Name the blood parasite species.
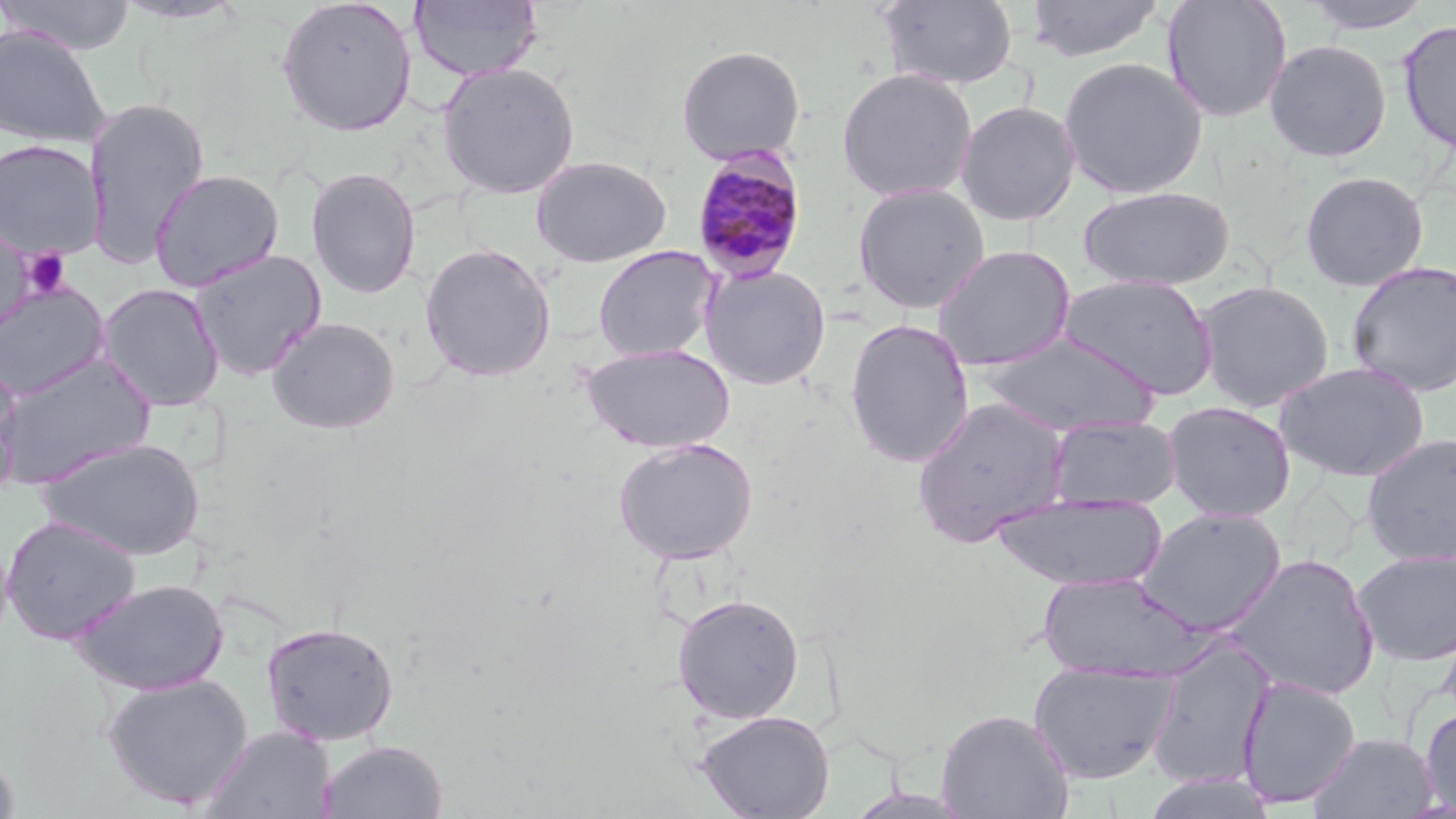
Plasmodium malariae.

field of view = one of a larger specimen
platelet locations = approximate bounding boxes as named x1/y1/x2/y2 corners in pixels: (x1=20, y1=248, x2=72, y2=299)
Plasmodium malariae-infected red blood cell locations = approximate bounding boxes as named x1/y1/x2/y2 corners in pixels: (x1=690, y1=147, x2=809, y2=284)
magnification = 1000x
stain = May-Grünwald-Giemsa
image size = 1456×819 pixels
modality = optical microscopy
preparation = thin blood smear
uninfected red blood cell locations = approximate bounding boxes as named x1/y1/x2/y2 corners in pixels: (x1=0, y1=0, x2=137, y2=55), (x1=112, y1=0, x2=248, y2=25), (x1=275, y1=0, x2=418, y2=138), (x1=408, y1=0, x2=544, y2=83), (x1=878, y1=0, x2=1019, y2=90), (x1=1025, y1=0, x2=1165, y2=63), (x1=1161, y1=0, x2=1293, y2=124), (x1=1298, y1=0, x2=1435, y2=34), (x1=1397, y1=19, x2=1456, y2=156), (x1=0, y1=24, x2=111, y2=148), (x1=1264, y1=39, x2=1392, y2=163), (x1=675, y1=44, x2=806, y2=166), (x1=1058, y1=56, x2=1209, y2=200), (x1=437, y1=61, x2=581, y2=200), (x1=836, y1=67, x2=978, y2=203), (x1=83, y1=97, x2=211, y2=269), (x1=955, y1=100, x2=1081, y2=226), (x1=0, y1=139, x2=106, y2=260), (x1=530, y1=155, x2=671, y2=268), (x1=305, y1=167, x2=421, y2=299), (x1=149, y1=169, x2=285, y2=292), (x1=1298, y1=170, x2=1430, y2=291), (x1=852, y1=182, x2=990, y2=313), (x1=1077, y1=186, x2=1237, y2=291), (x1=0, y1=219, x2=33, y2=342), (x1=419, y1=243, x2=556, y2=382), (x1=933, y1=244, x2=1076, y2=372), (x1=592, y1=245, x2=719, y2=362), (x1=189, y1=249, x2=327, y2=380), (x1=1345, y1=260, x2=1456, y2=397), (x1=700, y1=264, x2=832, y2=390), (x1=1057, y1=274, x2=1220, y2=401), (x1=1193, y1=279, x2=1335, y2=412), (x1=0, y1=281, x2=110, y2=400), (x1=96, y1=283, x2=226, y2=411), (x1=267, y1=316, x2=401, y2=434), (x1=844, y1=319, x2=975, y2=469), (x1=976, y1=333, x2=1161, y2=436), (x1=580, y1=343, x2=736, y2=453), (x1=0, y1=353, x2=156, y2=488), (x1=0, y1=360, x2=23, y2=496), (x1=1274, y1=361, x2=1431, y2=481), (x1=911, y1=396, x2=1071, y2=548), (x1=1162, y1=401, x2=1296, y2=523), (x1=1047, y1=416, x2=1182, y2=511), (x1=1360, y1=432, x2=1456, y2=566), (x1=37, y1=437, x2=206, y2=561), (x1=613, y1=437, x2=759, y2=564), (x1=991, y1=493, x2=1166, y2=590), (x1=1134, y1=506, x2=1287, y2=635), (x1=1, y1=514, x2=141, y2=645), (x1=1352, y1=548, x2=1456, y2=666), (x1=1225, y1=553, x2=1381, y2=701), (x1=1037, y1=571, x2=1205, y2=683), (x1=71, y1=577, x2=230, y2=695), (x1=672, y1=592, x2=805, y2=724), (x1=261, y1=621, x2=399, y2=746), (x1=1146, y1=636, x2=1276, y2=790), (x1=1028, y1=661, x2=1178, y2=784), (x1=101, y1=673, x2=253, y2=809), (x1=1236, y1=675, x2=1361, y2=808), (x1=1420, y1=703, x2=1456, y2=816), (x1=936, y1=707, x2=1074, y2=819), (x1=695, y1=710, x2=834, y2=819), (x1=200, y1=724, x2=336, y2=819), (x1=1308, y1=732, x2=1440, y2=818), (x1=318, y1=740, x2=448, y2=819), (x1=0, y1=750, x2=20, y2=818), (x1=1138, y1=771, x2=1278, y2=818)